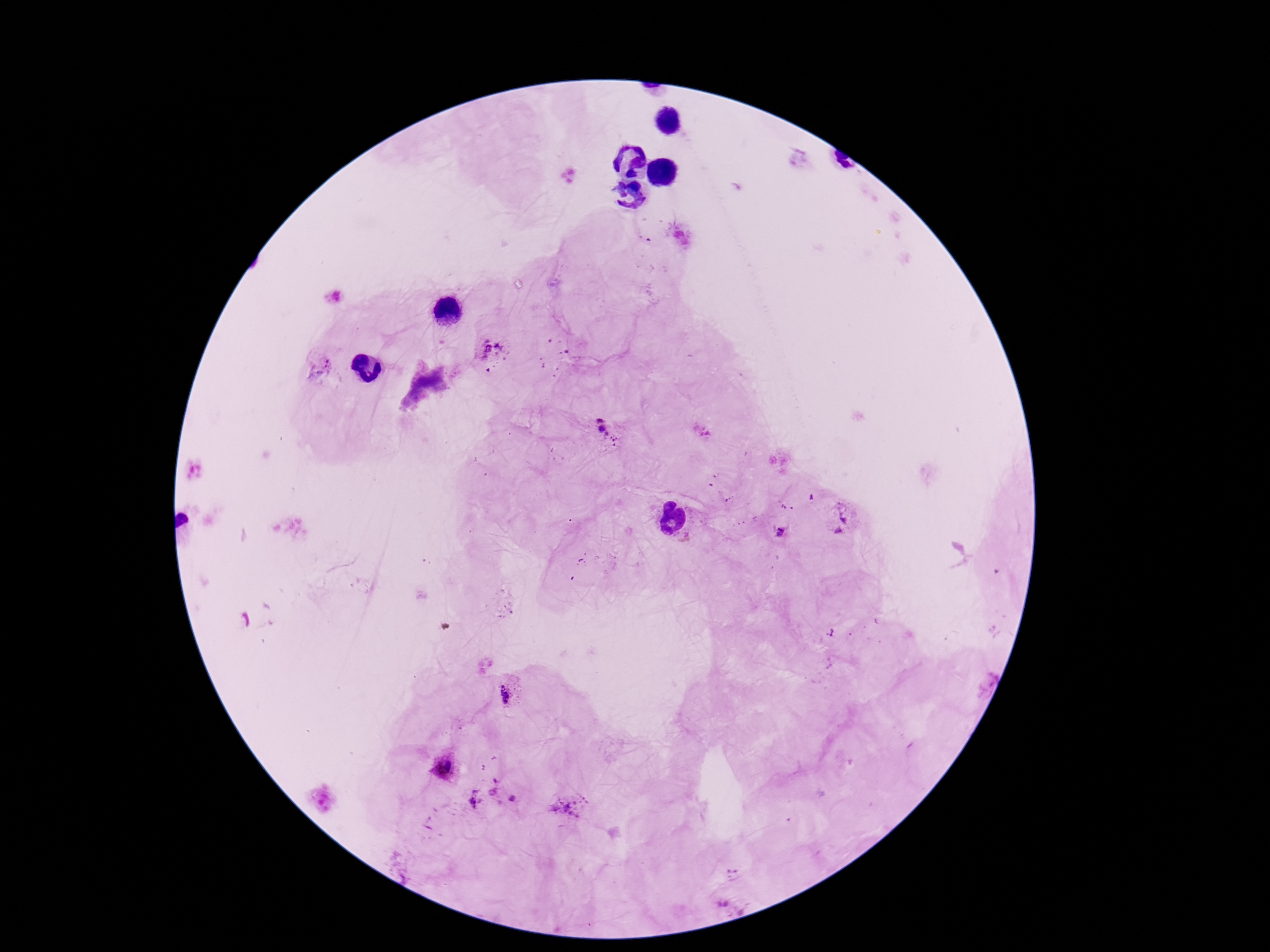
Approximate centers as {x, y} in pixels. Plasmodium parasite locations: {492, 348}, {321, 368}, {606, 428}, {840, 518}, {779, 533}, {507, 693}, {446, 768}, {504, 787}, {474, 799}, {570, 807}. Image is 1270×952 pixels. Smartphone photograph taken through the microscope eyepiece. Single field of view. 100x magnification. Giemsa stain. Patient malaria status: infected. Thick blood film.